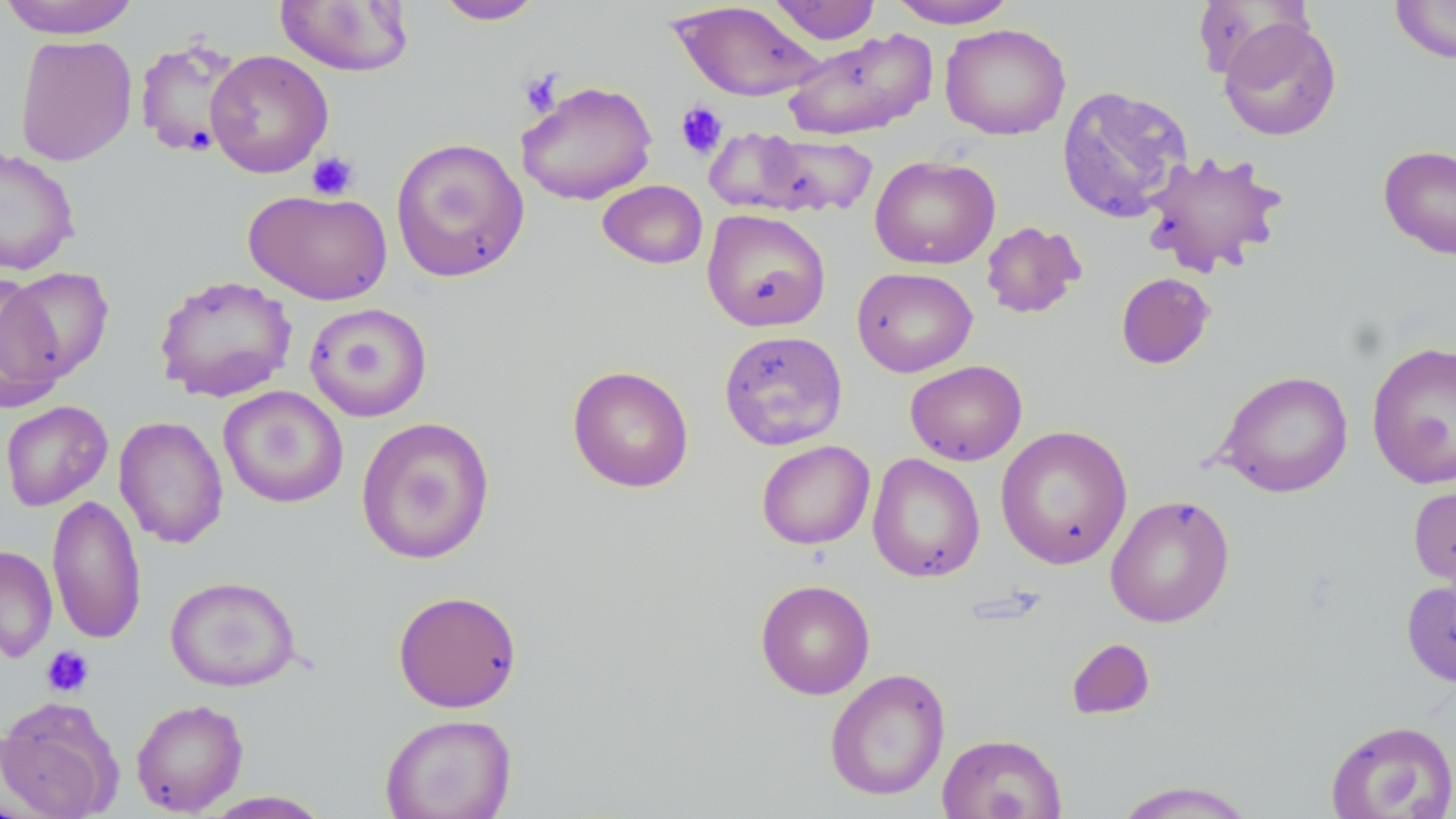

Summary:
  - Coordinate format: approximate bounding boxes as named x1/y1/x2/y2 corners in pixels
  - Uninfected red blood cell locations: (x1=0, y1=0, x2=143, y2=39), (x1=433, y1=0, x2=546, y2=25), (x1=767, y1=0, x2=881, y2=45), (x1=887, y1=0, x2=1018, y2=28), (x1=1390, y1=0, x2=1456, y2=64), (x1=274, y1=1, x2=415, y2=77), (x1=669, y1=1, x2=827, y2=103), (x1=1218, y1=17, x2=1341, y2=142), (x1=940, y1=23, x2=1071, y2=141), (x1=782, y1=29, x2=937, y2=141), (x1=14, y1=34, x2=137, y2=166), (x1=132, y1=35, x2=248, y2=159), (x1=205, y1=50, x2=333, y2=178), (x1=517, y1=80, x2=658, y2=206), (x1=1056, y1=81, x2=1193, y2=220), (x1=726, y1=130, x2=882, y2=218), (x1=390, y1=137, x2=530, y2=283), (x1=1378, y1=144, x2=1456, y2=260), (x1=0, y1=146, x2=82, y2=276), (x1=1139, y1=149, x2=1290, y2=278), (x1=870, y1=154, x2=1000, y2=270), (x1=597, y1=180, x2=708, y2=270), (x1=243, y1=188, x2=393, y2=306), (x1=702, y1=208, x2=831, y2=332), (x1=981, y1=220, x2=1086, y2=319), (x1=3, y1=267, x2=114, y2=381), (x1=852, y1=267, x2=978, y2=377), (x1=1115, y1=272, x2=1215, y2=369), (x1=0, y1=274, x2=67, y2=414), (x1=154, y1=274, x2=297, y2=403), (x1=304, y1=303, x2=432, y2=421), (x1=718, y1=330, x2=848, y2=451), (x1=1366, y1=340, x2=1456, y2=489), (x1=905, y1=360, x2=1027, y2=466), (x1=567, y1=365, x2=694, y2=493), (x1=1215, y1=370, x2=1354, y2=498), (x1=218, y1=385, x2=348, y2=508), (x1=0, y1=400, x2=113, y2=511), (x1=114, y1=416, x2=229, y2=549), (x1=355, y1=416, x2=496, y2=564), (x1=995, y1=425, x2=1133, y2=569), (x1=756, y1=440, x2=875, y2=549), (x1=867, y1=452, x2=986, y2=583), (x1=1407, y1=479, x2=1456, y2=596), (x1=47, y1=494, x2=147, y2=645), (x1=1105, y1=495, x2=1235, y2=627), (x1=0, y1=545, x2=58, y2=663), (x1=165, y1=575, x2=302, y2=692), (x1=1401, y1=575, x2=1456, y2=688), (x1=755, y1=579, x2=875, y2=699), (x1=392, y1=590, x2=522, y2=713), (x1=1066, y1=638, x2=1156, y2=720), (x1=824, y1=668, x2=950, y2=801), (x1=0, y1=697, x2=124, y2=819), (x1=130, y1=698, x2=249, y2=816), (x1=379, y1=713, x2=517, y2=819), (x1=1325, y1=719, x2=1456, y2=819), (x1=936, y1=732, x2=1066, y2=819), (x1=1110, y1=780, x2=1259, y2=818), (x1=200, y1=790, x2=334, y2=818)
  - Platelet locations: (x1=518, y1=69, x2=564, y2=118), (x1=675, y1=102, x2=728, y2=160), (x1=306, y1=151, x2=359, y2=201), (x1=42, y1=646, x2=94, y2=698)
  - Slide-level diagnosis: negative for blood parasites
  - Field of view: single
  - Modality: optical microscopy
  - Preparation: thin blood film
  - Image size: 1456×819 pixels
  - Magnification: 1000x
  - Stain: May-Grünwald-Giemsa